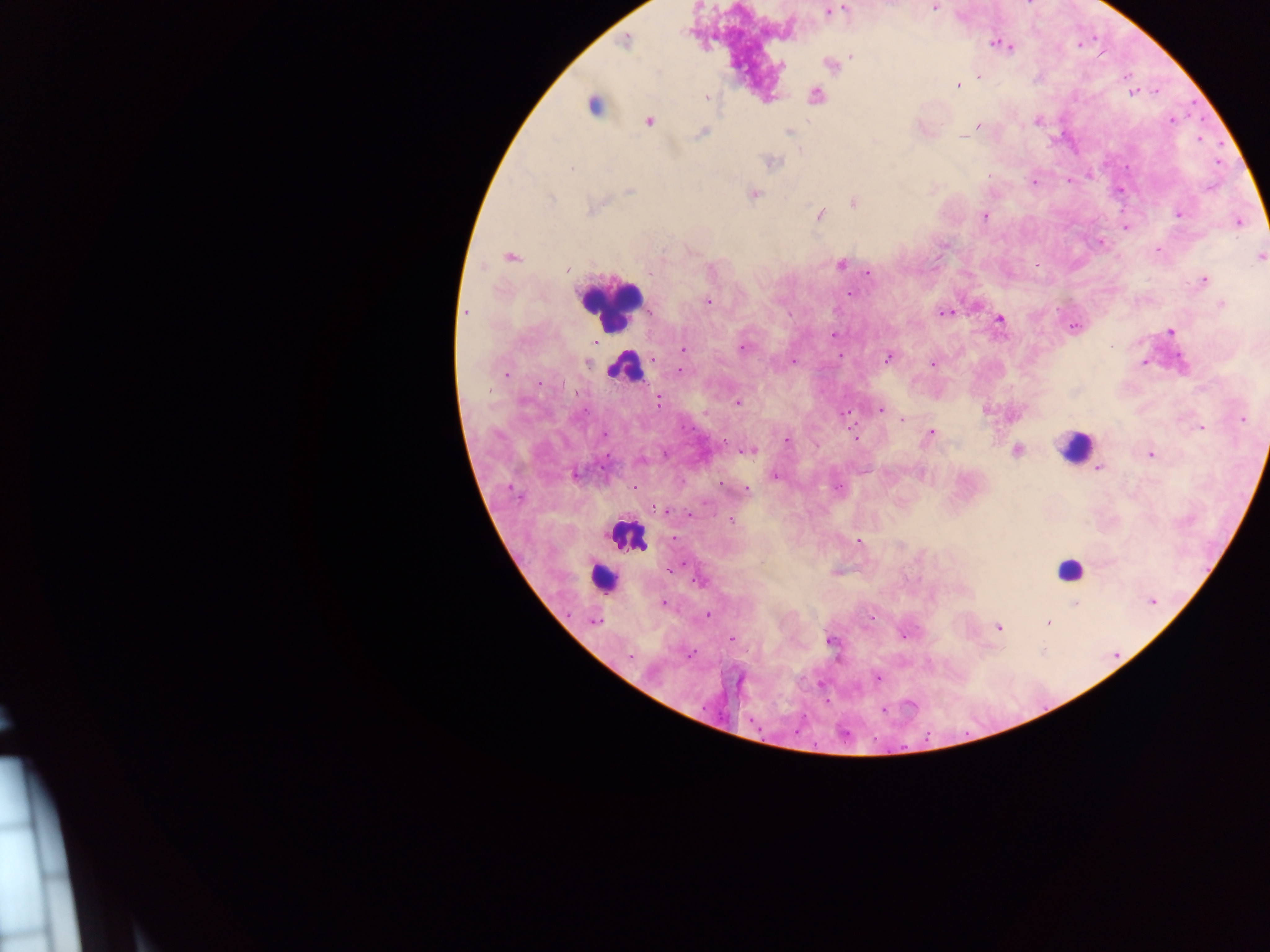
capture = mobile-phone photograph through a microscope
preparation = thick blood smear
country = Ghana
leukocyte locations = approximate centers as x y in pixels: 609 305; 626 370; 1074 446; 625 536; 1069 571; 603 579
field of view = single
Plasmodium parasite locations = approximate centers as x y in pixels: 934 7; 844 9; 828 12; 626 41; 998 44; 1008 47; 851 56; 781 66; 829 66; 979 76; 958 85; 1133 93; 815 96; 707 97; 593 106; 1171 120; 649 121; 1037 121; 978 126; 789 132; 700 133; 964 137; 800 149; 771 163; 571 168; 1034 183; 630 191; 754 193; 550 199; 853 203; 592 208; 1179 214; 820 215; 984 215; 1240 222; 1125 228; 1158 250; 510 257; 1260 257; 841 264; 566 270; 869 273; 1204 280; 850 293; 707 302; 1221 305; 466 312; 945 313; 1000 319; 1073 327; 1170 331; 833 334; 683 348; 742 348; 840 355; 888 357; 793 361; 588 363; 1143 363; 932 364; 681 371; 507 373; 658 402; 737 403; 880 410; 846 413; 903 419; 1242 419; 1201 428; 931 433; 604 435; 854 437; 786 441; 749 451; 1017 451; 1151 454; 1099 467; 576 475; 776 476; 745 490; 660 508; 666 510; 732 521; 858 541; 673 569; 699 581; 1152 602; 663 603; 1075 604; 708 615; 594 621; 1048 623; 999 627; 732 640; 831 640; 690 655; 630 656; 877 679
image size = 1270×952 pixels